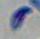
Micrograph. Toxoplasma gondii is seen. 1000x magnification.